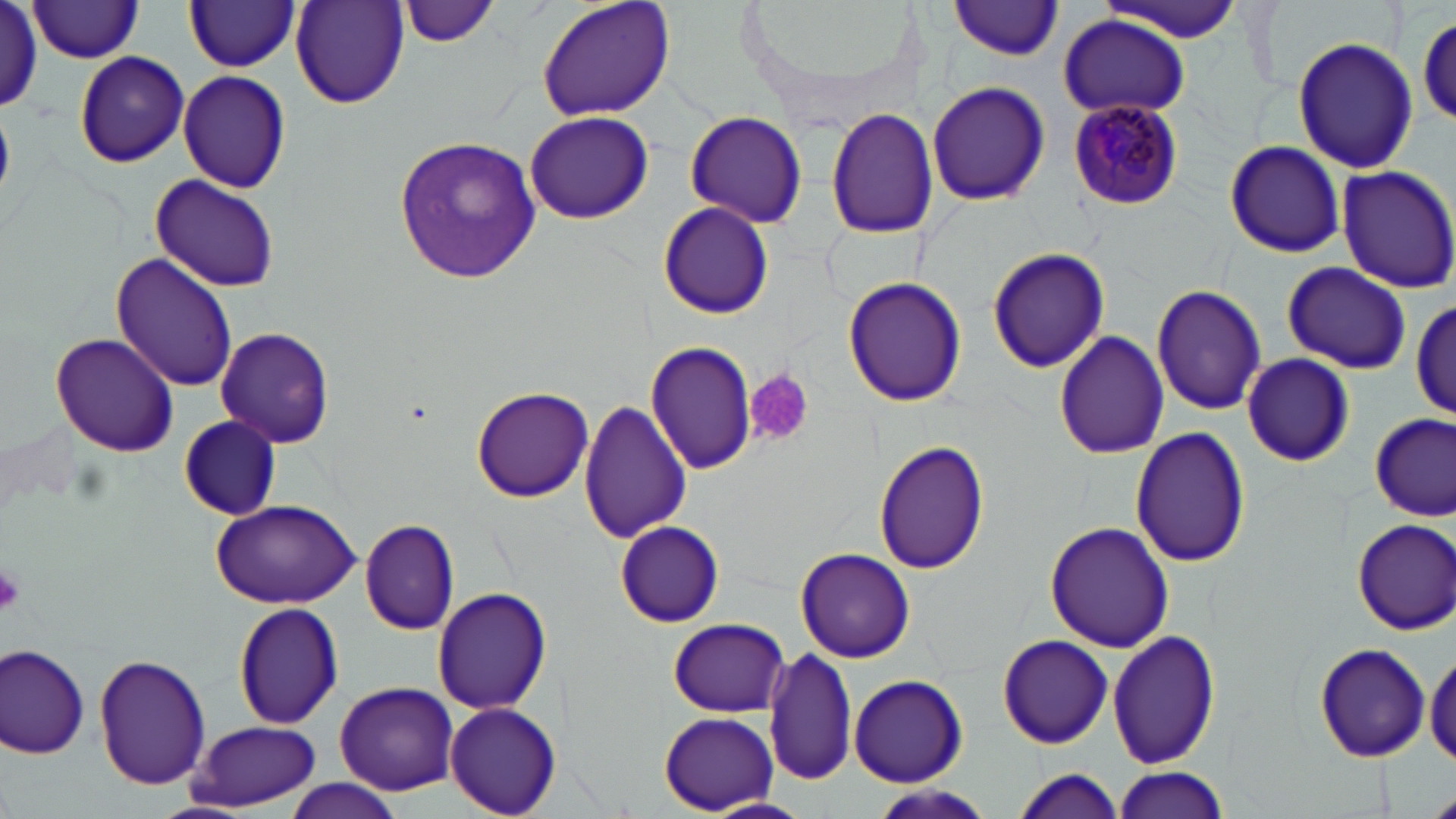
plasmodium_malariae_infected_red_blood_cell_locations: 'approximate bounding boxes as (x1, y1, x2, y2) in pixels: (1065, 99, 1183, 210)'
slide_level_diagnosis: Plasmodium malariae
stain: May-Grünwald-Giemsa
platelet_locations: 'approximate bounding boxes as (x1, y1, x2, y2) in pixels: (746, 370, 813, 445), (0, 563, 26, 615)'
modality: optical microscopy
uninfected_red_blood_cell_locations: 'approximate bounding boxes as (x1, y1, x2, y2) in pixels: (396, 0, 499, 49), (535, 0, 677, 122), (186, 1, 300, 72), (949, 1, 1065, 61), (1103, 1, 1247, 42), (27, 2, 146, 62), (290, 2, 410, 109), (0, 3, 47, 111), (1413, 11, 1455, 125), (1057, 14, 1193, 121), (1293, 37, 1419, 175), (74, 51, 190, 168), (178, 69, 292, 193), (926, 82, 1051, 208), (826, 106, 939, 240), (524, 109, 654, 225), (682, 110, 808, 227), (392, 132, 542, 283), (1221, 139, 1347, 259), (1334, 165, 1456, 293), (149, 173, 281, 293), (658, 201, 774, 320), (985, 246, 1109, 373), (111, 253, 236, 393), (1282, 261, 1412, 375), (843, 275, 967, 409), (1152, 284, 1267, 415), (1411, 294, 1456, 422), (215, 324, 335, 448), (1053, 330, 1169, 461), (50, 333, 181, 459), (644, 339, 758, 474), (1242, 353, 1354, 467), (471, 387, 593, 503), (577, 399, 690, 544), (1371, 412, 1455, 521), (176, 416, 283, 520), (1131, 425, 1250, 568), (875, 440, 991, 576), (210, 500, 363, 608), (1351, 517, 1456, 635), (358, 519, 460, 635), (1043, 520, 1174, 652), (615, 522, 725, 626), (795, 546, 916, 663), (432, 587, 552, 716), (235, 601, 343, 728), (665, 619, 793, 717), (1108, 628, 1221, 768), (997, 633, 1113, 750), (1, 642, 92, 758), (1314, 643, 1429, 761), (763, 645, 861, 787), (1426, 647, 1456, 767), (94, 653, 210, 791), (848, 673, 968, 786), (333, 681, 460, 794), (444, 702, 560, 816), (660, 712, 778, 813), (186, 720, 322, 811), (1111, 767, 1229, 818), (1008, 769, 1128, 818), (279, 782, 407, 818), (702, 797, 810, 819)'
field_of_view: one of a larger specimen
image_size: 1456×819 pixels
magnification: 1000x
preparation: thin blood smear